Assess this cell for malaria.
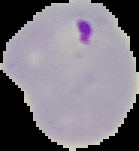

It is parasitized.

Image is 139×151 pixels. From a thin blood film. Segmented cell region on a black background.